Assess the morphology of the erythrocytes.
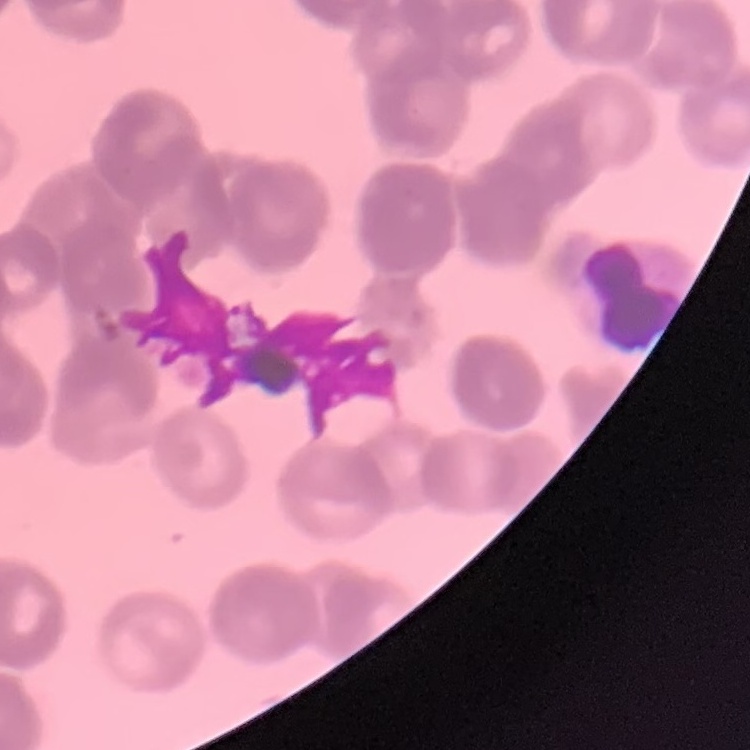

They show rouleaux formation.

Thin blood smear. One tile cut from a larger photomicrograph. Stained with either Field's or Giemsa.